Report the malaria status of this cell.
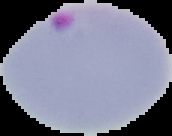

It is parasitized.

From a thin blood smear. Image is 172×136 pixels. Cell region segmented out of the field of view; the surrounding area is masked to black.